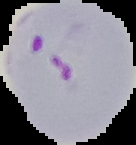
image type = segmented cell region with the area outside set to black
preparation = thin blood smear
image size = 136×145 pixels
malaria status = parasitized